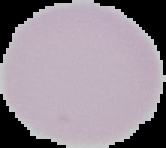
Cell region segmented out of the field of view; the surrounding area is masked to black. From a thin blood smear. Image is 166×148 pixels. Malaria status: uninfected.